Give the preparation type.
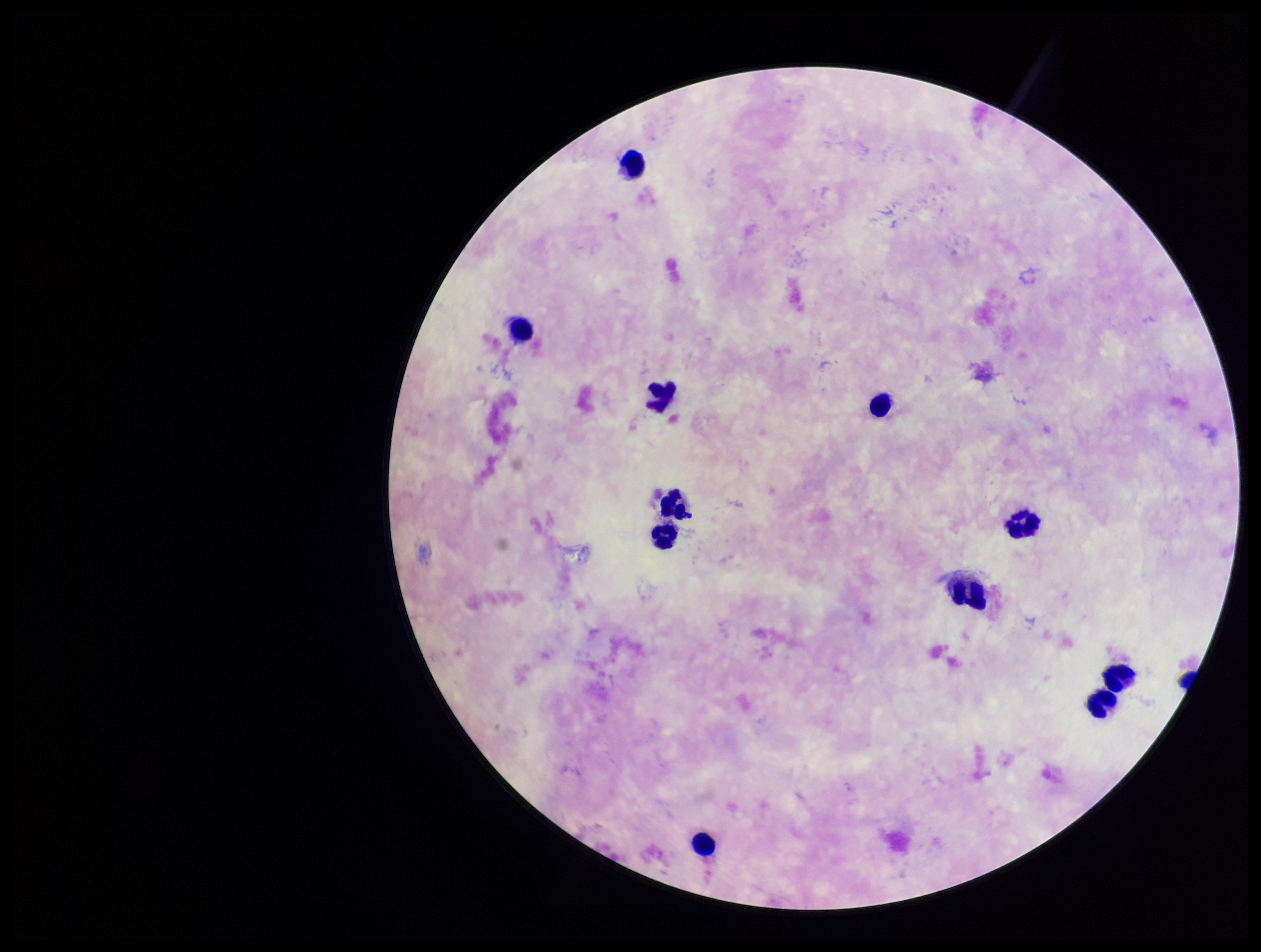

A thick smear.

Summary:
  - Image size: 1261×952 pixels
  - Capture: smartphone photograph through the microscope eyepiece
  - Patient malaria status: negative
  - Field of view: one from this slide
  - Leukocyte count: 11
  - Plasmodium parasites: none seen
  - Stain: Giemsa
  - Parasite count: 0